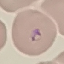

Summary:
  - Result: malaria parasites detected
  - Capture: smartphone through the microscope eyepiece
  - Stain: Giemsa
  - Preparation: thin blood smear
  - Image type: automatically extracted cell patch, resized to 64 × 64 pixels